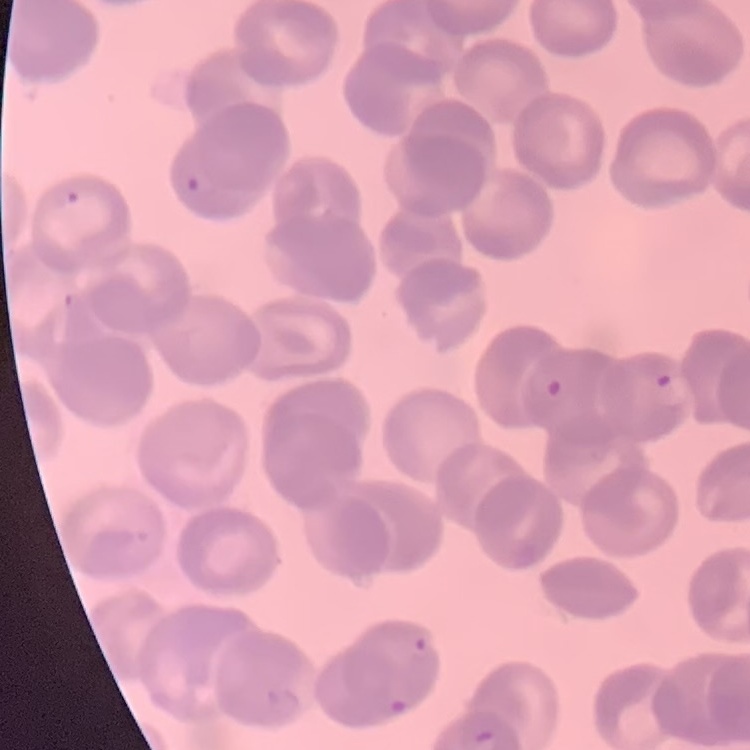
The erythrocytes show rouleaux formation. One tile cut from a larger photomicrograph. Thin blood smear. Stained with either Field's or Giemsa.